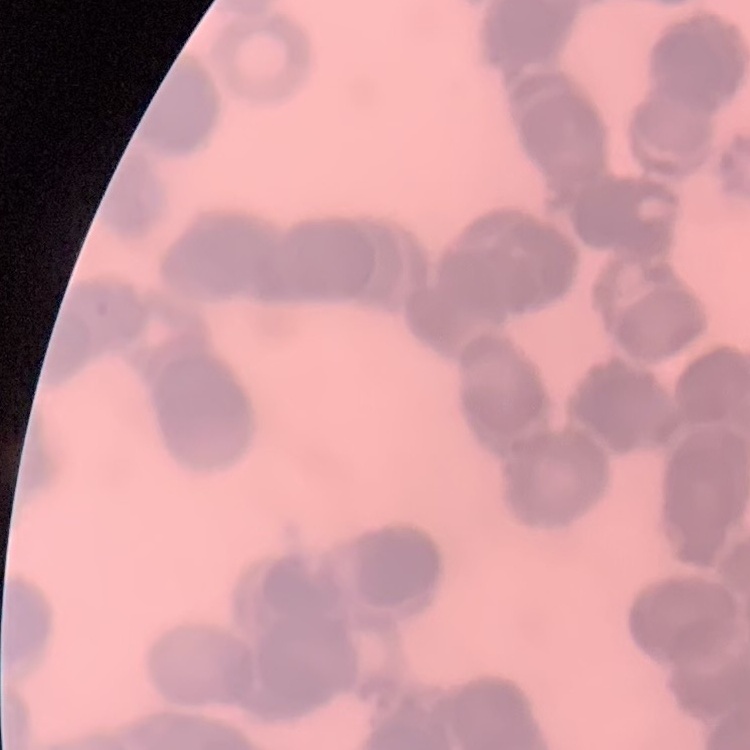

The erythrocytes exhibit rouleaux formation. Square crop of a larger photomicrograph. Thin peripheral smear. Stained with either Field's or Giemsa.